Outline each blood parasite and name the species.
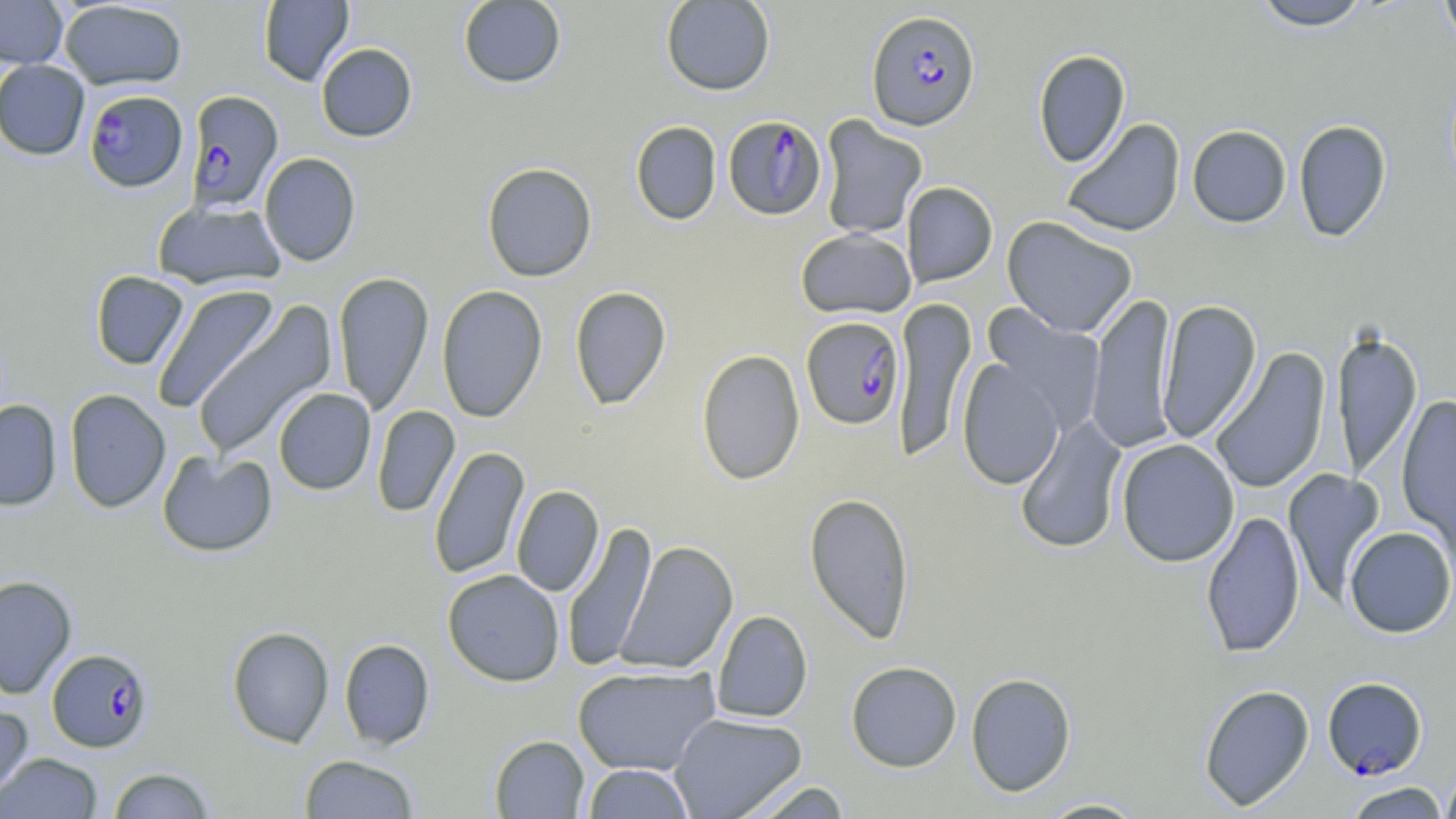

Approximate bounding boxes as (x1,y1)-(x2,y2) corner pairs in pixels.
Plasmodium falciparum-infected red blood cells: (866,9)-(980,130), (83,89)-(188,192), (185,90)-(284,213), (723,115)-(827,221), (801,316)-(905,430), (47,648)-(153,752), (1322,676)-(1427,779).
No Plasmodium ovale, Plasmodium malariae, Plasmodium vivax, Babesia divergens, or Trypanosoma brucei observed.

Summary:
  - Uninfected red blood cell locations: (0,0)-(67,68), (258,0)-(354,86), (457,0)-(567,89), (660,0)-(776,96), (1252,0)-(1372,31), (1438,0)-(1456,52), (58,1)-(187,91), (315,43)-(418,142), (1033,49)-(1130,168), (0,59)-(90,160), (818,115)-(928,240), (1062,118)-(1186,238), (1293,119)-(1392,242), (630,120)-(722,226), (1187,124)-(1291,228), (259,153)-(361,267), (482,162)-(597,282), (901,181)-(998,287), (152,200)-(286,289), (1002,215)-(1138,338), (796,228)-(917,319), (90,271)-(189,370), (333,271)-(434,416), (151,285)-(280,414), (436,285)-(547,422), (569,286)-(671,410), (1086,293)-(1179,453), (891,298)-(977,464), (1156,299)-(1262,445), (190,302)-(337,459), (981,305)-(1107,437), (1331,329)-(1422,482), (1209,347)-(1332,495), (696,349)-(805,486), (957,358)-(1066,490), (64,388)-(171,513), (273,388)-(376,495), (1396,395)-(1456,550), (0,400)-(62,511), (372,405)-(460,517), (1014,416)-(1127,555), (1116,439)-(1239,567), (429,445)-(530,581), (157,450)-(277,558), (1282,469)-(1386,607), (511,485)-(604,597), (804,491)-(915,644), (1200,510)-(1305,659), (561,520)-(657,672), (1343,526)-(1456,638), (615,540)-(739,676), (442,569)-(565,687), (0,575)-(77,699), (712,610)-(812,723), (227,626)-(334,747), (339,638)-(435,750), (846,661)-(962,772), (572,665)-(720,776), (965,672)-(1077,796), (1198,683)-(1315,810), (0,705)-(34,805), (669,712)-(807,819), (489,735)-(590,818), (1,753)-(102,818), (300,754)-(420,818), (582,763)-(695,818), (108,766)-(216,818), (1440,767)-(1456,819), (738,779)-(854,819), (1343,781)-(1451,819), (1032,797)-(1151,818)
  - Slide-level diagnosis: Plasmodium falciparum
  - Field of view: single
  - Modality: optical microscopy
  - Stain: May-Grünwald-Giemsa
  - Preparation: thin blood film
  - Image size: 1456×819 pixels
  - Magnification: 1000x